State the preparation type.
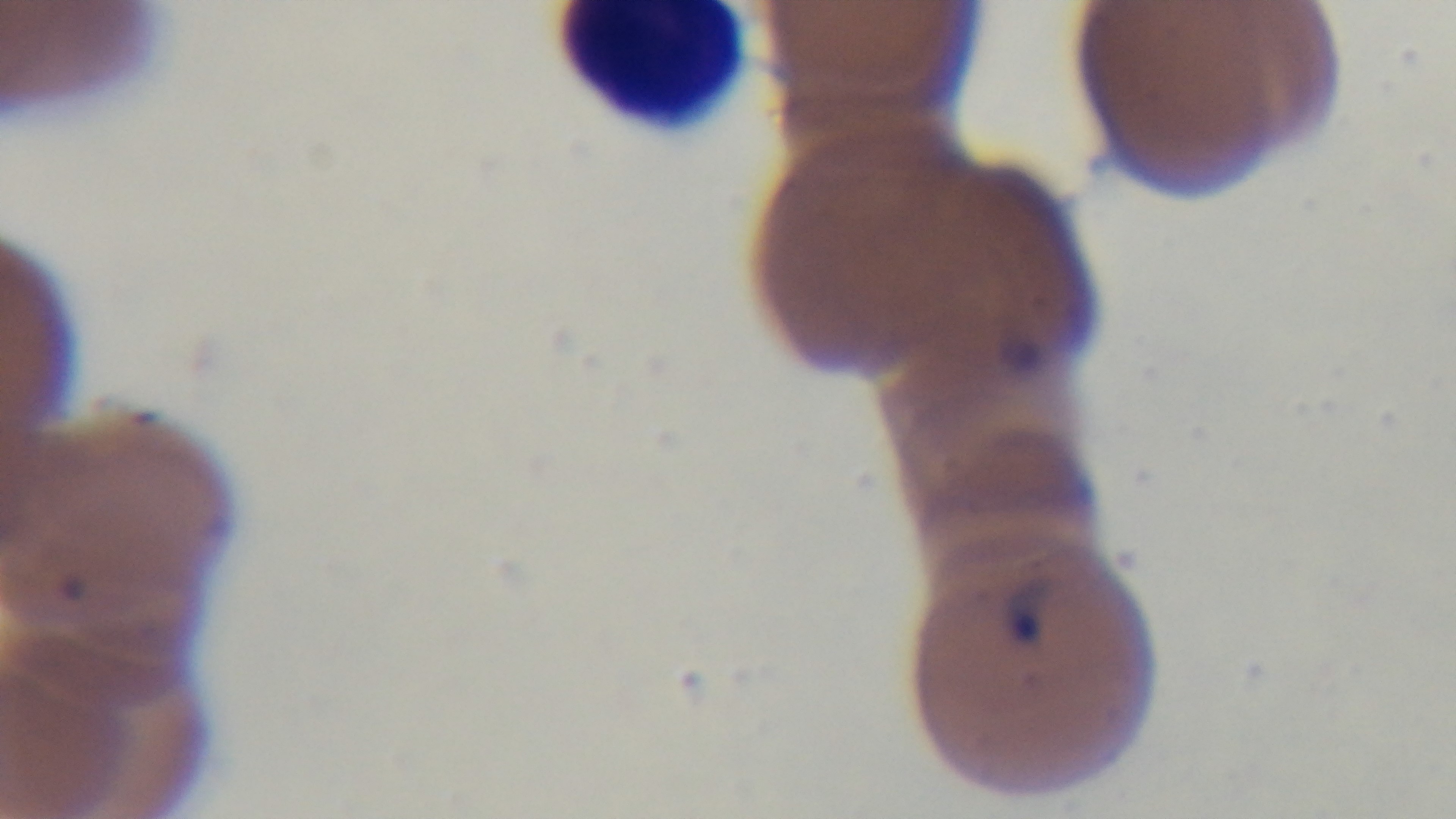
It is a thin blood film.

100x oil-immersion objective. Single field of view. Captured with a mounted 4K digital camera. Giemsa-stained. Malaria status: infected. Photomicrograph.